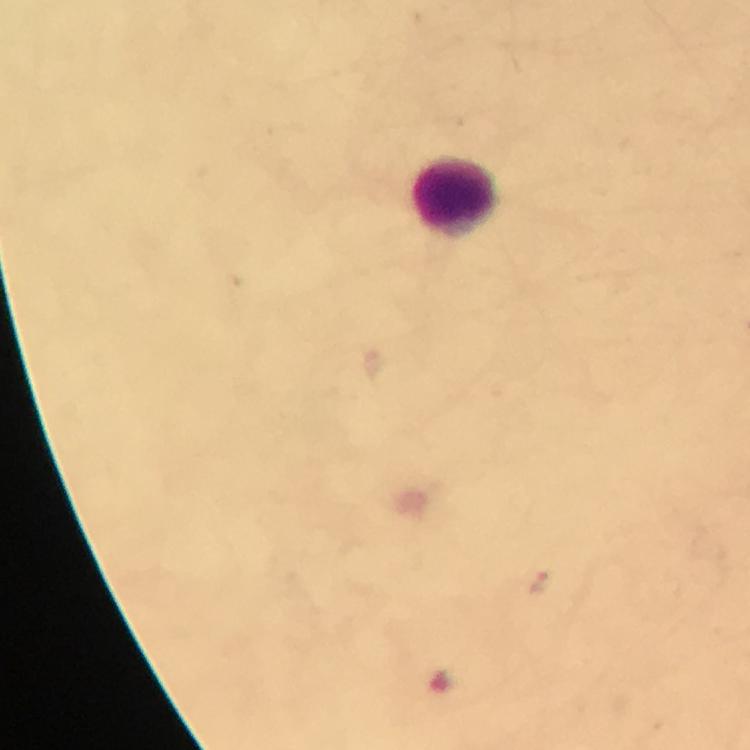
{
  "preparation": "thick blood film",
  "malaria_parasite_locations": "approximate centers as {x, y} in pixels: {540, 584}, {440, 679}",
  "context": "from a diagnostic examination for malaria",
  "stain": "Giemsa",
  "image_size": "750×750 pixels",
  "cropped_from": "one field of view",
  "capture": "smartphone photograph through a microscope",
  "immersion_oil": "applied",
  "leukocyte_locations": "approximate centers as {x, y} in pixels: {456, 197}",
  "magnification": "100x"
}